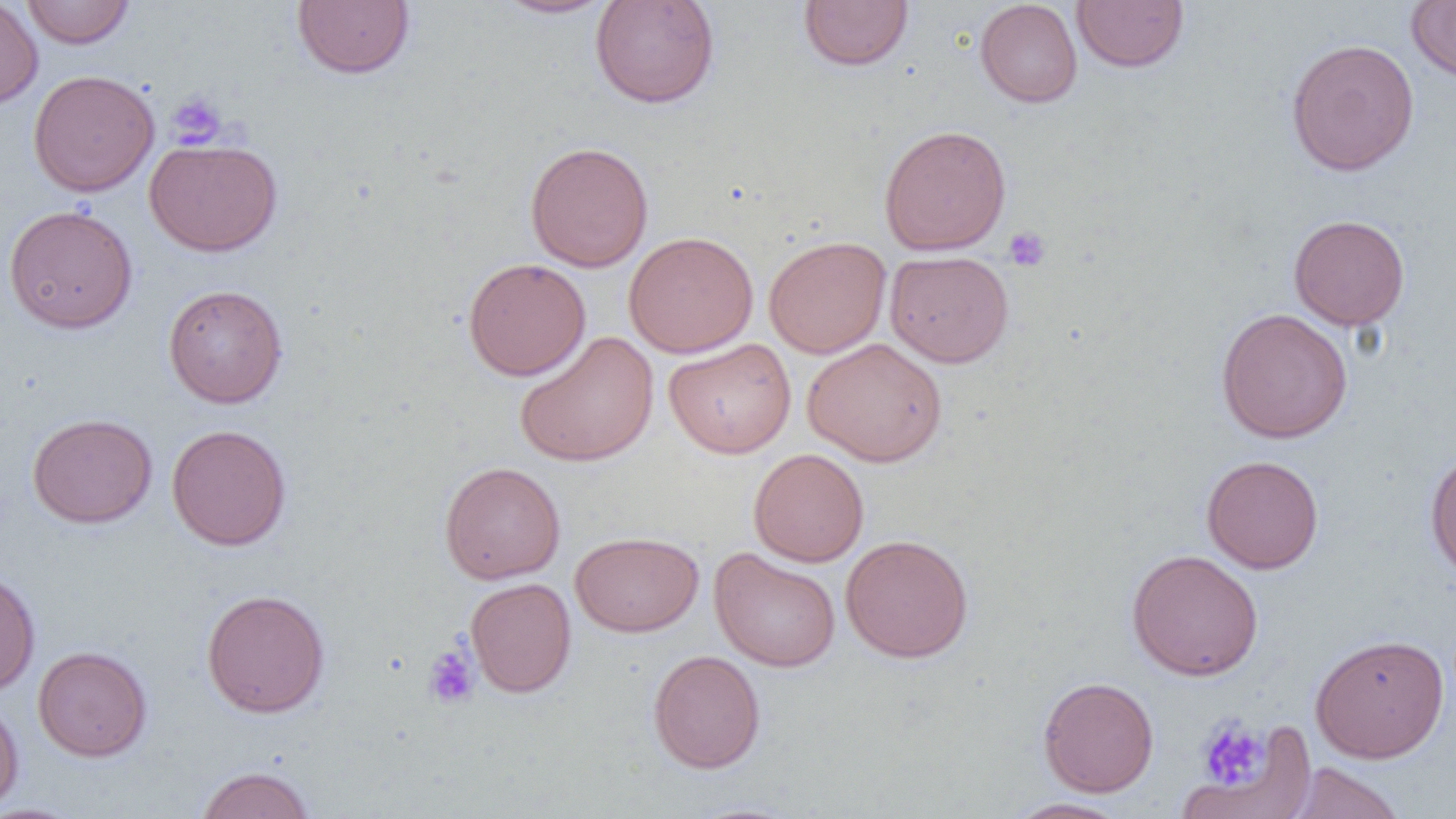

slide-level diagnosis = negative for blood parasites
magnification = 1000x
preparation = thin blood film
image size = 1456×819 pixels
uninfected red blood cell locations = approximate bounding boxes as (x1, y1, x2, y2) in pixels: (0, 0, 43, 109), (292, 0, 415, 79), (490, 0, 618, 19), (589, 0, 720, 109), (799, 0, 914, 71), (1071, 0, 1190, 72), (1406, 0, 1456, 82), (20, 1, 135, 48), (974, 1, 1083, 107), (1285, 38, 1420, 176), (28, 69, 159, 197), (879, 124, 1011, 255), (144, 138, 282, 257), (525, 141, 654, 272), (4, 204, 138, 333), (1288, 213, 1410, 330), (623, 231, 759, 358), (763, 235, 891, 359), (885, 250, 1014, 368), (462, 257, 591, 380), (163, 284, 288, 408), (1215, 307, 1353, 443), (514, 330, 659, 467), (802, 337, 947, 467), (664, 338, 796, 459), (27, 412, 158, 528), (166, 423, 292, 550), (1424, 447, 1456, 581), (748, 448, 869, 567), (1202, 455, 1324, 574), (439, 461, 566, 584), (569, 531, 704, 637), (840, 533, 974, 663), (709, 547, 841, 672), (1126, 549, 1264, 681), (0, 568, 40, 697), (465, 577, 576, 697), (201, 588, 331, 717), (1310, 632, 1450, 763), (33, 645, 152, 761), (647, 649, 766, 773), (1038, 676, 1159, 797), (0, 696, 25, 817), (1194, 716, 1282, 801), (1288, 762, 1406, 819), (195, 765, 315, 818), (1003, 798, 1130, 818)
field of view = single
modality = optical microscopy
platelet locations = approximate bounding boxes as (x1, y1, x2, y2) in pixels: (167, 91, 227, 148), (1003, 226, 1051, 272), (423, 642, 480, 709), (1198, 719, 1268, 789)